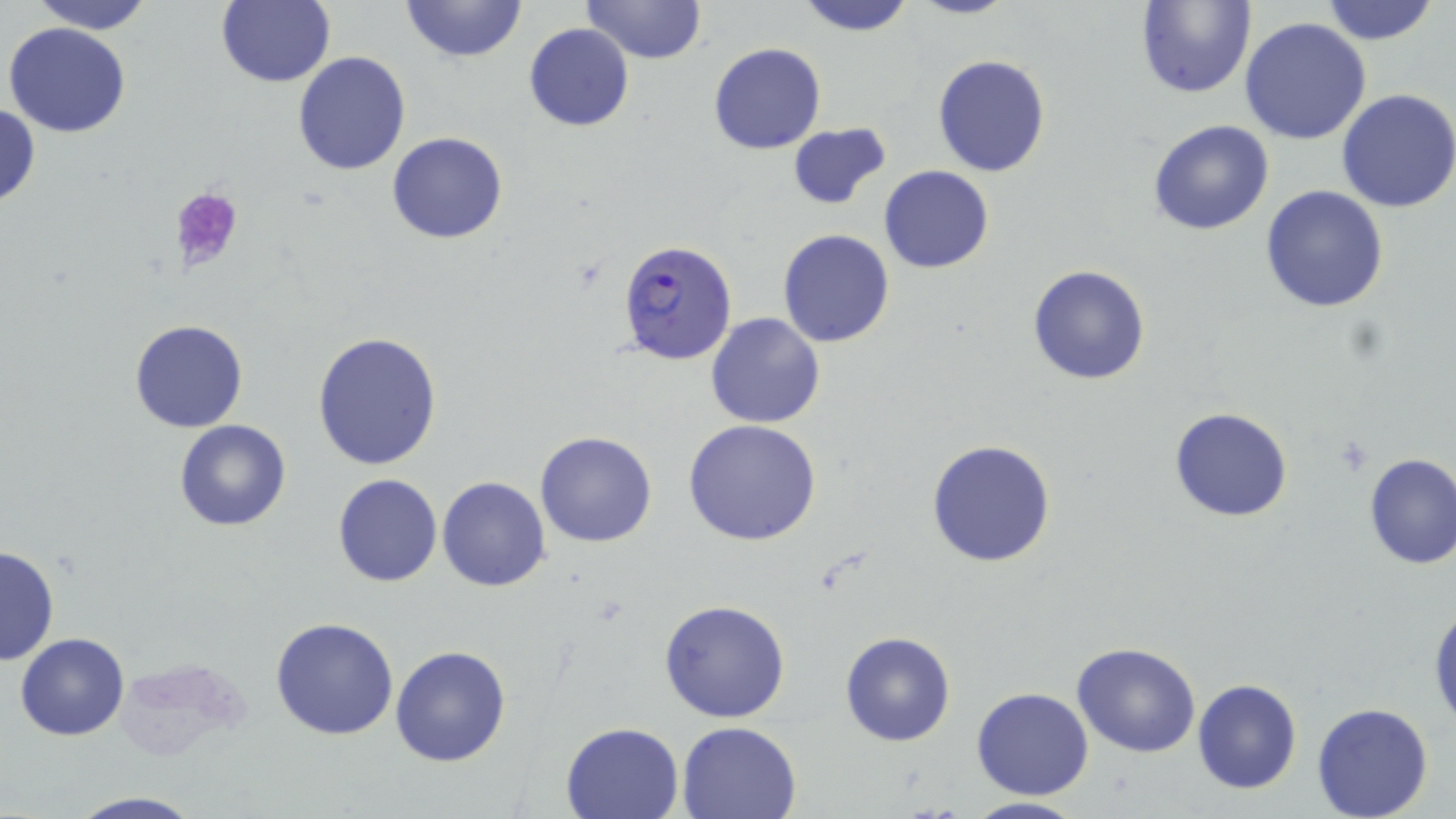

Approximate bounding boxes as named x1/y1/x2/y2 corners in pixels. Plasmodium falciparum-infected red blood cell locations: (x1=618, y1=240, x2=739, y2=365). Uninfected red blood cell locations: (x1=28, y1=0, x2=155, y2=33), (x1=400, y1=0, x2=528, y2=64), (x1=583, y1=0, x2=708, y2=63), (x1=794, y1=0, x2=915, y2=35), (x1=906, y1=0, x2=1016, y2=20), (x1=1135, y1=0, x2=1256, y2=99), (x1=1318, y1=0, x2=1440, y2=45), (x1=213, y1=1, x2=336, y2=88), (x1=1239, y1=17, x2=1372, y2=144), (x1=4, y1=21, x2=131, y2=137), (x1=523, y1=23, x2=634, y2=132), (x1=707, y1=42, x2=826, y2=155), (x1=292, y1=50, x2=411, y2=177), (x1=933, y1=54, x2=1051, y2=176), (x1=1335, y1=89, x2=1456, y2=212), (x1=0, y1=101, x2=41, y2=213), (x1=1148, y1=120, x2=1275, y2=236), (x1=786, y1=122, x2=892, y2=211), (x1=386, y1=132, x2=509, y2=244), (x1=880, y1=165, x2=994, y2=274), (x1=1261, y1=186, x2=1390, y2=314), (x1=777, y1=229, x2=895, y2=348), (x1=1027, y1=264, x2=1151, y2=385), (x1=705, y1=310, x2=826, y2=430), (x1=130, y1=320, x2=249, y2=433), (x1=312, y1=331, x2=443, y2=471), (x1=1169, y1=407, x2=1293, y2=523), (x1=682, y1=418, x2=823, y2=546), (x1=174, y1=419, x2=292, y2=531), (x1=535, y1=430, x2=657, y2=547), (x1=925, y1=439, x2=1057, y2=569), (x1=1361, y1=452, x2=1456, y2=569), (x1=331, y1=473, x2=443, y2=587), (x1=436, y1=475, x2=551, y2=593), (x1=0, y1=544, x2=60, y2=667), (x1=658, y1=600, x2=790, y2=722), (x1=1429, y1=602, x2=1456, y2=736), (x1=270, y1=617, x2=399, y2=739), (x1=840, y1=631, x2=955, y2=746), (x1=15, y1=632, x2=129, y2=740), (x1=1072, y1=641, x2=1202, y2=757), (x1=390, y1=644, x2=512, y2=767), (x1=1192, y1=679, x2=1303, y2=795), (x1=971, y1=686, x2=1093, y2=800), (x1=1311, y1=701, x2=1434, y2=819), (x1=676, y1=720, x2=803, y2=818), (x1=560, y1=721, x2=686, y2=818), (x1=65, y1=792, x2=206, y2=818), (x1=959, y1=796, x2=1089, y2=819). Platelet locations: (x1=171, y1=186, x2=245, y2=273). Slide-level diagnosis: Plasmodium falciparum. May-Grünwald-Giemsa-stained preparation. Captured at 1000x magnification. Image is 1456×819 pixels. Thin blood smear. Single field of view. Optical microscopy.